Classify the preparation.
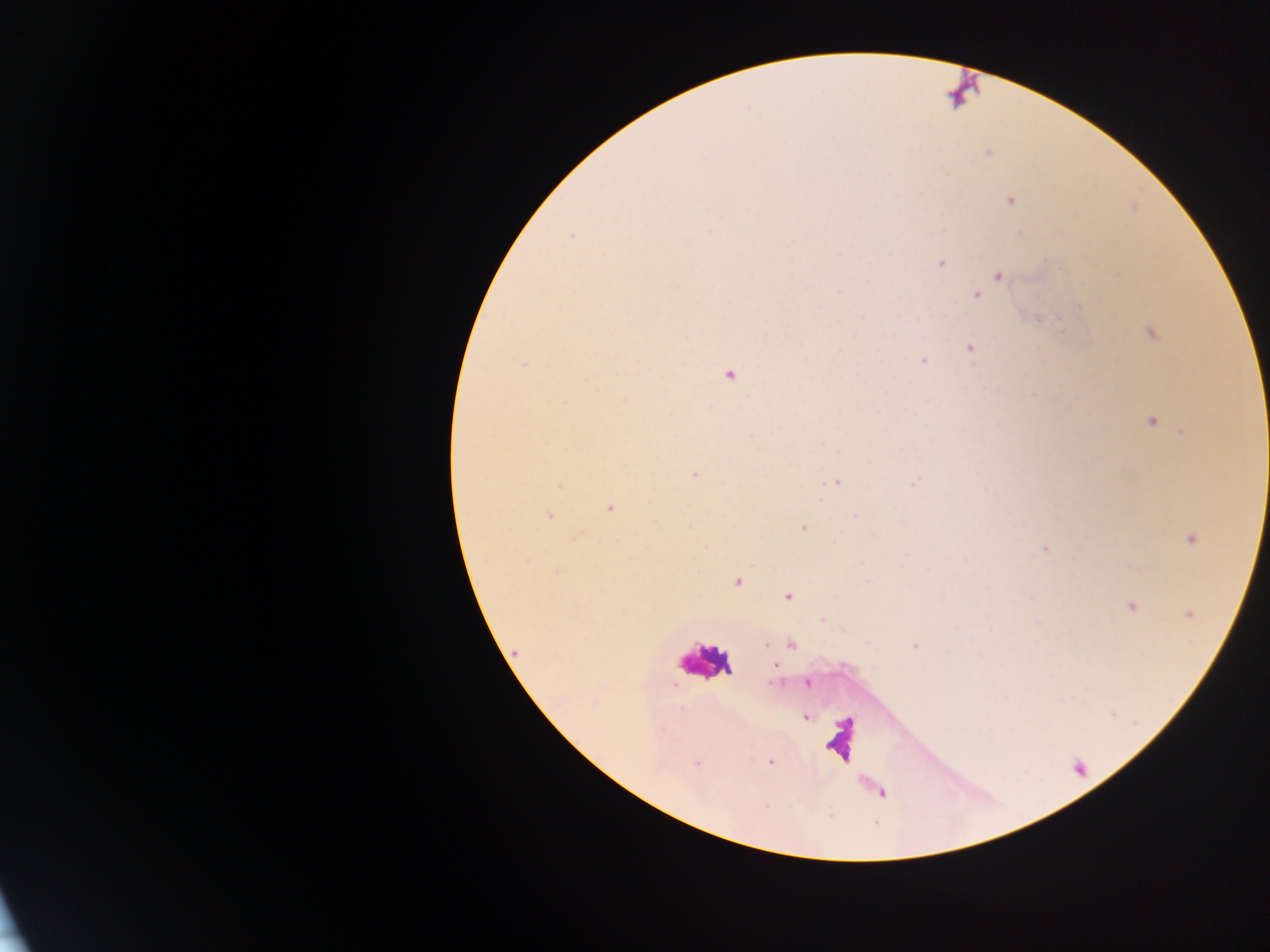

This is a thick smear.

Approximate centers as {x, y} in pixels. Malaria parasite locations: {988, 152}, {1010, 200}, {571, 234}, {940, 263}, {997, 275}, {976, 295}, {1150, 332}, {970, 346}, {923, 360}, {523, 364}, {727, 375}, {1152, 420}, {693, 473}, {836, 481}, {914, 482}, {560, 485}, {609, 508}, {549, 515}, {803, 528}, {1190, 537}, {1044, 549}, {1133, 566}, {736, 581}, {788, 597}, {1131, 606}, {1187, 613}, {764, 644}, {790, 644}, {915, 646}, {806, 683}, {804, 717}, {771, 761}. Leukocyte locations: {702, 661}, {840, 740}. Collected in Ghana. Photographed through a microscope with a mobile-phone camera. Image is 1270×952 pixels. One field of view.